Report the malaria status of this cell.
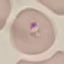

It is parasitized.

capture: smartphone through the microscope eyepiece
image_type: cell patch, automatically extracted from a larger field of view and resized to 64 × 64 pixels
preparation: thin smear
stain: Giemsa